Assess this cell for malaria.
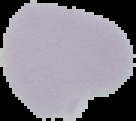
It is uninfected.

preparation = thin blood film
image size = 136×121 pixels
image type = segmented cell region on a black background